Name the cell type shown.
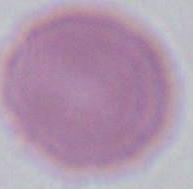

This is an erythrocyte.

Summary:
  - Magnification: 1000x
  - Modality: photomicrograph